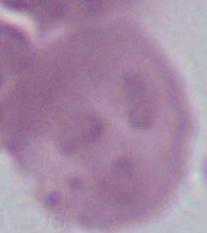
An erythrocyte is shown. Micrograph. 1000x magnification.